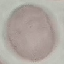
Summary:
  - Result: no malaria parasites seen
  - Capture: smartphone through the microscope eyepiece
  - Preparation: thin blood film
  - Image type: automatically extracted cell patch, resized to 64 × 64 pixels
  - Stain: Giemsa